Locate every Plasmodium parasite and every leukocyte.
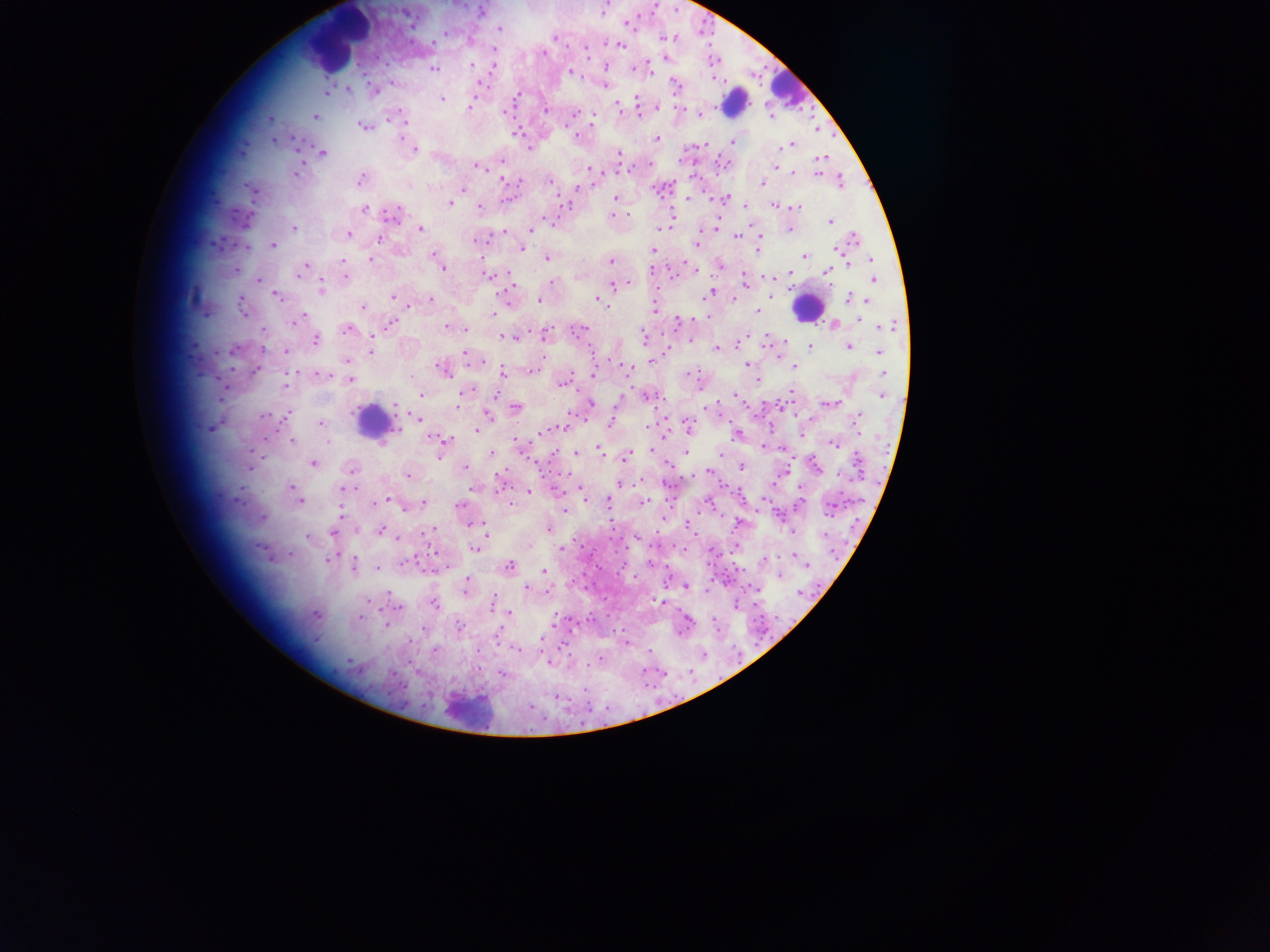

Approximate centers as (x, y) in pixels.
Plasmodium parasites: (602, 9), (480, 12), (406, 15), (626, 23), (411, 25), (498, 29), (446, 32), (555, 37), (471, 41), (432, 44), (620, 44), (494, 50), (664, 58), (472, 66), (492, 67), (606, 67), (433, 68), (632, 68), (570, 72), (604, 79), (479, 83), (674, 83), (604, 84), (348, 88), (372, 90), (326, 91), (441, 99), (636, 99), (617, 106), (469, 107), (656, 107), (678, 109), (545, 110), (637, 110), (574, 112), (698, 114), (314, 115), (401, 119), (591, 120), (404, 124), (363, 125), (815, 129), (517, 134), (576, 136), (274, 138), (655, 139), (734, 141), (790, 144), (704, 145), (415, 148), (528, 148), (321, 152), (618, 154), (821, 157), (502, 160), (476, 166), (298, 167), (773, 168), (590, 169), (629, 169), (791, 171), (817, 171), (360, 179), (503, 179), (840, 180), (550, 181), (593, 184), (762, 184), (253, 189), (463, 189), (616, 198), (687, 199), (726, 199), (448, 202), (745, 205), (774, 205), (479, 206), (795, 207), (364, 209), (392, 214), (244, 217), (613, 217), (549, 219), (671, 219), (829, 220), (293, 228), (420, 228), (789, 228), (659, 229), (530, 230), (760, 232), (348, 234), (503, 234), (734, 234), (381, 236), (854, 239), (477, 240), (696, 243), (272, 244), (521, 248), (836, 248), (757, 249), (653, 250), (805, 255), (435, 256), (547, 258), (870, 258), (371, 259), (610, 260), (717, 264), (848, 264), (440, 265), (303, 267), (826, 270), (672, 274), (743, 274), (345, 275), (487, 275), (788, 275), (577, 276), (769, 277), (258, 280), (743, 280), (873, 281), (550, 282), (613, 284), (321, 290), (710, 292), (276, 294), (506, 294), (393, 296), (429, 298), (733, 298), (597, 299), (848, 299), (539, 300), (868, 300), (408, 305), (242, 306), (363, 307), (654, 309), (757, 313), (297, 319), (695, 319), (678, 321), (834, 324), (391, 325), (889, 325), (455, 326), (447, 327), (348, 328), (582, 328), (464, 329), (263, 332), (545, 335), (507, 336), (766, 337), (643, 338), (691, 338), (316, 340), (737, 345), (810, 346), (847, 346), (717, 348), (234, 349), (285, 351), (371, 351), (878, 352), (466, 353), (776, 353), (347, 361), (652, 361), (748, 364), (794, 367), (627, 368), (257, 369), (442, 369), (533, 370), (503, 373), (592, 374), (883, 374), (323, 375), (757, 377), (350, 379), (562, 382), (286, 386), (464, 390), (791, 391), (495, 393), (420, 394), (881, 395), (648, 396), (736, 396), (590, 403), (830, 403), (742, 405), (781, 405), (455, 407), (515, 407), (285, 414), (488, 415), (265, 416), (417, 419), (856, 420), (566, 421), (320, 423), (609, 423), (647, 426), (564, 427), (687, 427), (211, 428), (476, 430), (541, 431), (665, 431), (800, 433), (737, 435), (443, 439), (291, 441), (833, 444), (519, 446), (765, 447), (598, 448), (650, 449), (784, 449), (685, 451), (440, 454), (491, 454), (574, 454), (719, 454), (626, 455), (313, 463), (536, 463), (741, 465), (668, 466), (816, 466), (464, 467), (351, 469), (709, 471), (408, 475), (500, 477), (619, 485), (474, 487), (290, 488), (344, 489), (554, 489), (580, 489), (528, 492), (386, 500), (298, 501), (377, 501), (641, 502), (424, 503), (607, 503), (511, 504), (458, 505), (798, 505), (830, 506), (404, 507), (565, 510), (263, 518), (663, 519), (481, 523), (738, 523), (471, 524), (688, 524), (548, 529), (380, 530), (429, 530), (791, 531), (334, 533), (485, 533), (307, 535), (528, 545), (476, 548), (432, 549), (560, 549), (792, 554), (330, 558), (765, 559), (409, 562), (650, 563), (353, 565), (805, 565), (508, 566), (378, 568), (544, 571), (780, 576), (685, 585), (466, 587), (755, 588), (526, 589), (708, 589), (388, 593), (661, 603), (434, 604), (735, 605), (396, 606), (315, 613), (509, 613), (360, 617), (685, 619), (385, 623), (459, 628), (422, 629), (626, 642), (562, 645), (516, 648), (549, 661), (502, 673), (584, 688), (556, 696).
Leukocytes: (335, 41), (788, 87), (734, 102), (807, 308), (374, 423), (466, 712).

image size = 1270×952 pixels
capture = mobile-phone photograph through a microscope
country = Ghana
preparation = thick blood smear
field of view = single